State which parasite is depicted.
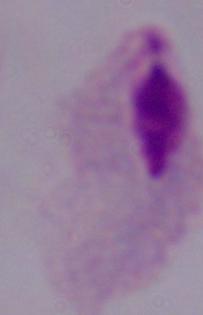
A trichomonad.

Captured at 1000x magnification. Photomicrograph.